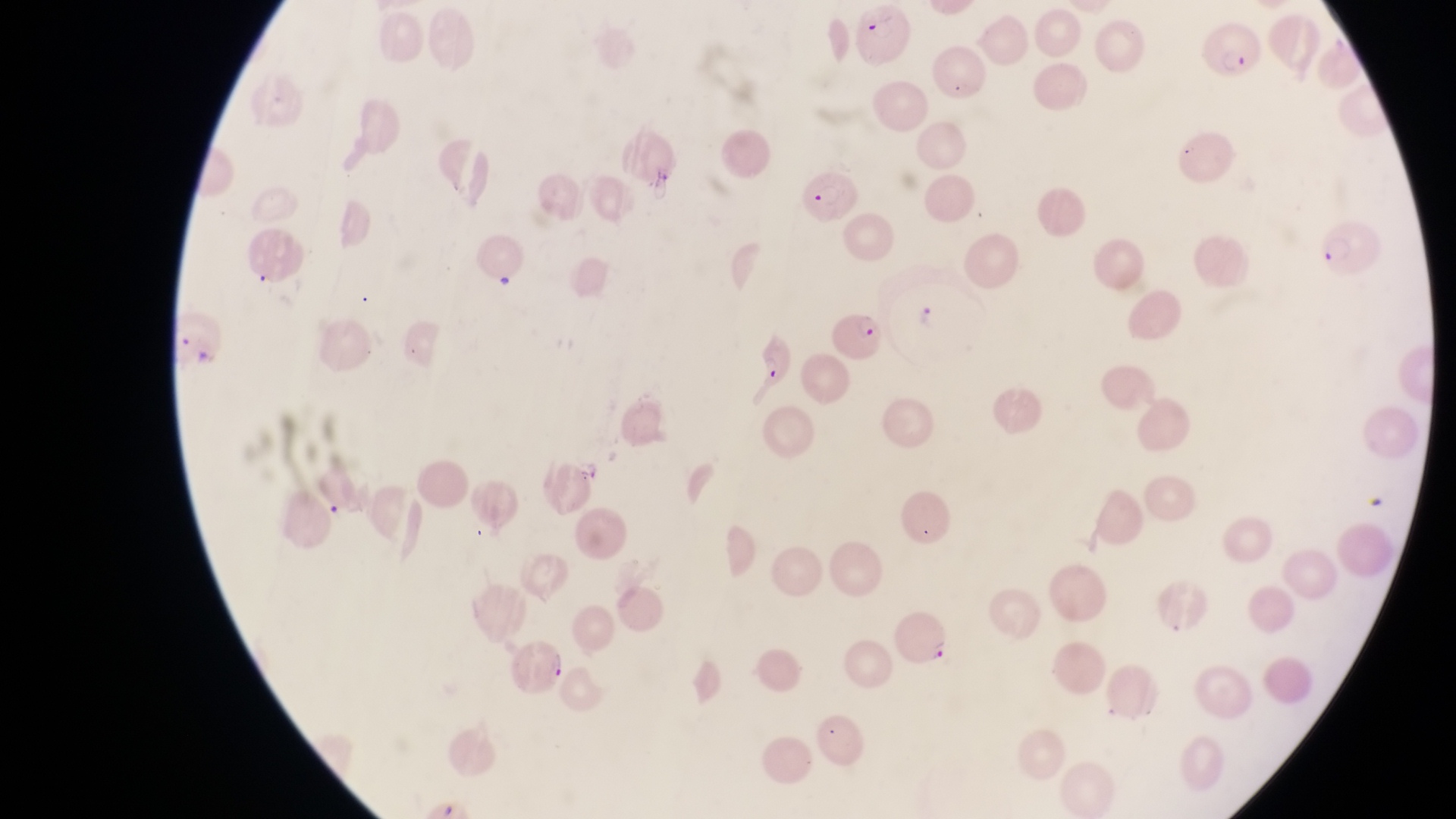
Approximate bounding boxes as left top right bottom in pixels.
Summary:
  - Parasitised red blood cell locations: 616 132 683 184; 798 169 867 225; 829 301 898 373; 748 334 798 390; 888 610 957 666; 513 635 567 688
  - Field of view: single
  - Country: Uganda
  - Preparation: thin blood smear
  - Capture: smartphone photograph through the eyepiece of an Olympus CX-23 microscope
  - Image size: 1456×819 pixels
  - Magnification: 1000x